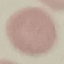

Summary:
  - Malaria status: uninfected
  - Stain: Giemsa
  - Capture: smartphone camera at the microscope eyepiece
  - Image type: cell patch, automatically extracted from a larger field of view and resized to 64 × 64 pixels
  - Preparation: thin blood film